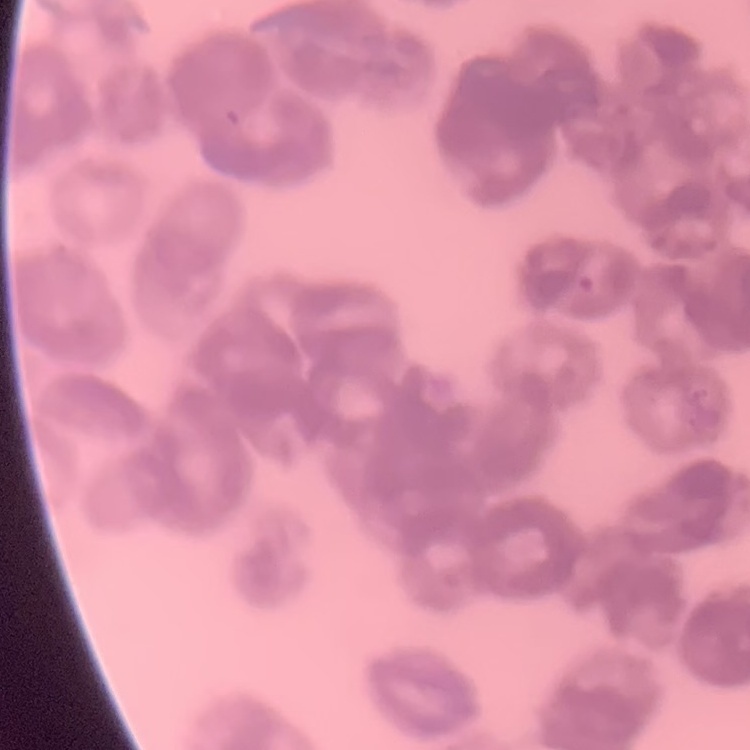
The red blood cells exhibit rouleaux formation. Square crop of a larger photomicrograph. Field's or Giemsa stain. Thin blood smear.